Locate every Plasmodium falciparum-infected red blood cell.
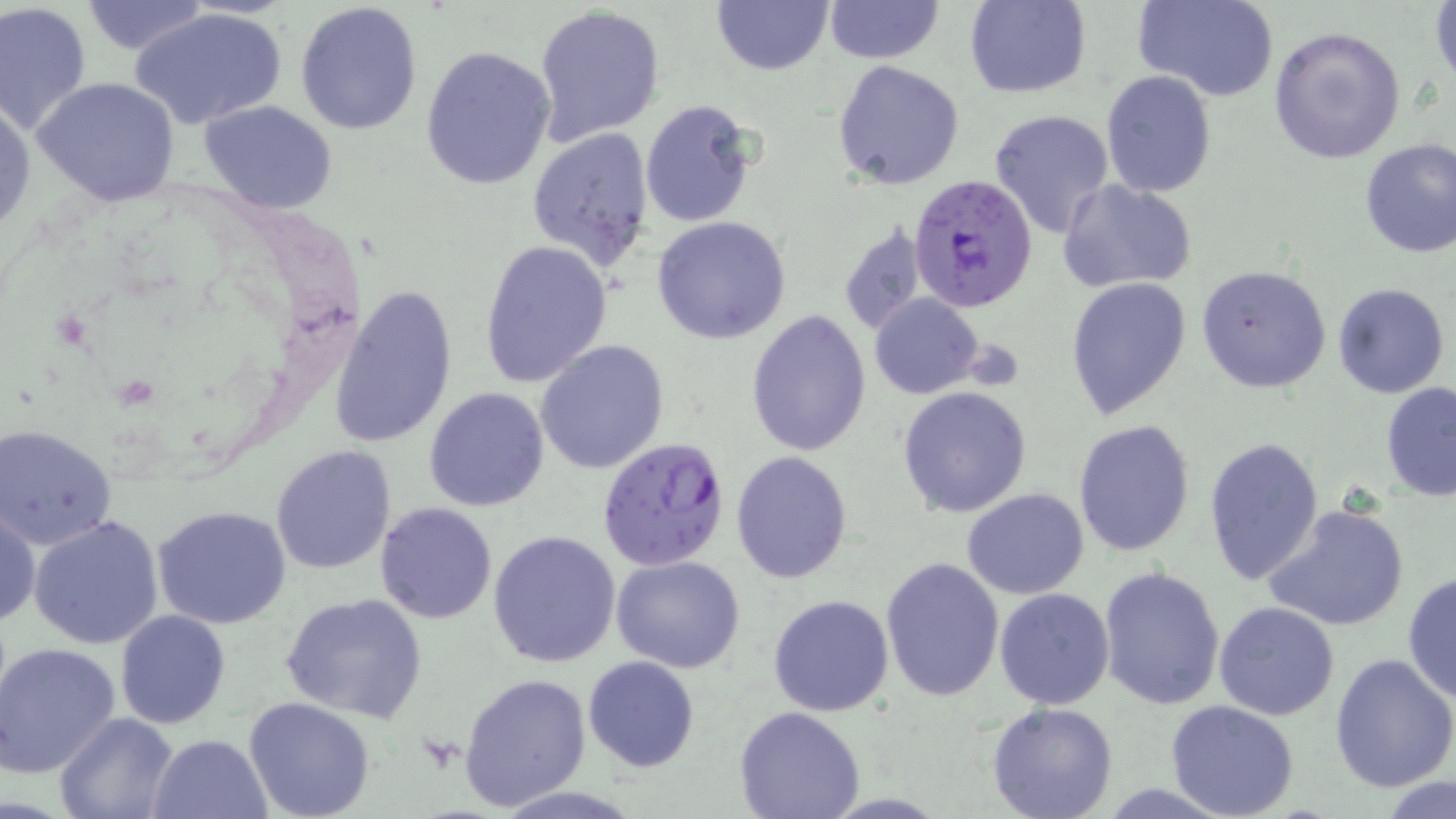
Approximate bounding boxes as (x1, y1, x2, y2) in pixels.
Plasmodium falciparum-infected red blood cells: (908, 175, 1038, 310), (597, 434, 731, 572).

slide-level diagnosis = Plasmodium falciparum
stain = May-Grünwald-Giemsa
modality = optical microscopy
magnification = 1000x
uninfected red blood cell locations = approximate bounding boxes as (x1, y1, x2, y2) in pixels: (711, 0, 834, 76), (823, 0, 943, 65), (963, 0, 1091, 98), (1137, 0, 1279, 102), (79, 1, 210, 55), (295, 1, 423, 137), (1430, 1, 1456, 89), (1, 3, 94, 137), (533, 4, 666, 147), (133, 8, 287, 131), (1268, 25, 1404, 163), (420, 45, 556, 190), (833, 60, 964, 189), (1101, 70, 1216, 196), (34, 77, 182, 209), (0, 97, 35, 236), (198, 100, 338, 215), (640, 100, 758, 229), (988, 108, 1115, 240), (526, 126, 656, 271), (1358, 138, 1456, 259), (1057, 179, 1198, 295), (652, 216, 791, 343), (836, 220, 929, 336), (478, 239, 612, 387), (1195, 265, 1332, 393), (1066, 277, 1192, 420), (330, 283, 459, 449), (1332, 284, 1450, 399), (870, 293, 984, 399), (745, 309, 872, 456), (535, 340, 669, 475), (1380, 382, 1456, 501), (897, 385, 1034, 518), (423, 387, 551, 512), (1072, 419, 1197, 559), (1, 423, 119, 549), (1202, 436, 1324, 587), (270, 445, 398, 573), (731, 450, 853, 583), (962, 488, 1090, 599), (374, 502, 497, 623), (1263, 503, 1410, 633), (1, 505, 41, 629), (153, 505, 294, 629), (30, 515, 164, 649), (488, 529, 623, 668), (611, 555, 745, 674), (879, 557, 1005, 703), (1096, 565, 1224, 710), (1402, 573, 1456, 703), (994, 588, 1115, 710), (279, 592, 428, 723), (768, 594, 895, 717), (1213, 601, 1342, 720), (115, 610, 231, 730), (0, 641, 122, 778), (1330, 654, 1456, 795), (582, 656, 702, 773), (459, 673, 592, 812), (243, 696, 377, 819), (1165, 700, 1299, 819), (986, 702, 1119, 819), (733, 707, 865, 819), (55, 711, 180, 818), (147, 734, 273, 819), (1379, 778, 1454, 819)
image size = 1456×819 pixels
field of view = single
preparation = thin blood smear